Name the blood parasite species.
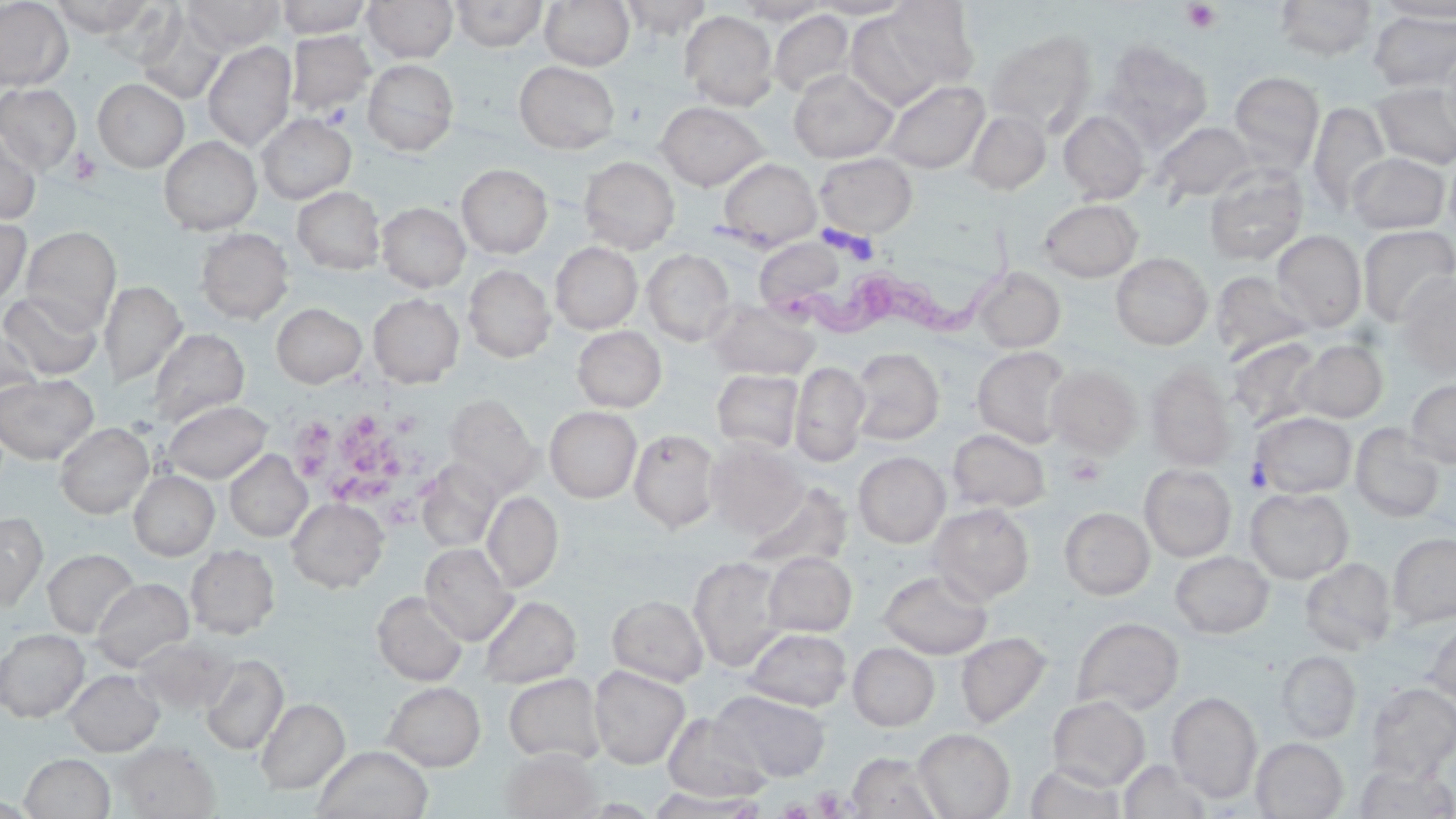

Trypanosoma brucei.

Approximate bounding boxes as (x1, y1, x2, y2) in pixels. Uninfected red blood cell locations: (0, 0, 73, 91), (50, 0, 156, 36), (183, 0, 284, 53), (274, 0, 373, 38), (363, 0, 458, 62), (451, 0, 547, 51), (540, 0, 634, 70), (619, 0, 712, 38), (808, 0, 916, 19), (881, 0, 981, 92), (1274, 0, 1377, 61), (734, 1, 831, 25), (1377, 1, 1456, 21), (844, 8, 956, 111), (768, 9, 856, 99), (1368, 9, 1456, 92), (680, 11, 778, 110), (137, 12, 227, 105), (986, 29, 1097, 136), (286, 30, 375, 116), (1102, 40, 1212, 146), (203, 41, 296, 151), (1439, 41, 1456, 145), (363, 59, 459, 155), (514, 61, 620, 153), (788, 69, 898, 163), (1229, 71, 1325, 173), (93, 79, 188, 171), (880, 79, 989, 174), (1372, 81, 1456, 169), (0, 82, 81, 172), (656, 101, 768, 190), (1308, 101, 1391, 213), (966, 109, 1051, 195), (1059, 110, 1150, 204), (257, 114, 356, 203), (1154, 121, 1256, 204), (0, 130, 41, 225), (159, 136, 261, 234), (1444, 148, 1456, 238), (1346, 152, 1451, 234), (815, 153, 917, 239), (579, 156, 679, 253), (718, 158, 821, 249), (457, 164, 553, 258), (1204, 166, 1309, 265), (293, 186, 385, 274), (1039, 199, 1142, 281), (377, 202, 470, 292), (0, 214, 31, 307), (1357, 225, 1456, 326), (21, 226, 121, 331), (196, 228, 293, 323), (1272, 230, 1367, 331), (754, 237, 849, 315), (551, 242, 642, 333), (642, 249, 735, 345), (1111, 253, 1213, 349), (463, 265, 554, 362), (972, 266, 1066, 352), (1211, 271, 1312, 360), (1395, 272, 1456, 378), (99, 280, 186, 387), (0, 291, 102, 380), (368, 293, 464, 387), (707, 300, 820, 380), (271, 302, 367, 388), (0, 325, 43, 410), (573, 326, 666, 412), (146, 328, 249, 426), (1227, 337, 1322, 429), (1293, 339, 1388, 423), (972, 346, 1072, 447), (851, 347, 944, 445), (790, 361, 869, 466), (1047, 364, 1141, 456), (1146, 364, 1235, 470), (711, 369, 804, 453), (0, 373, 98, 463), (1405, 377, 1456, 468), (445, 395, 541, 494), (163, 399, 271, 483), (545, 407, 641, 502), (1252, 411, 1356, 497), (55, 422, 153, 518), (1350, 424, 1446, 523), (947, 428, 1051, 513), (629, 429, 720, 532), (705, 439, 806, 537), (225, 451, 311, 541), (853, 451, 950, 547), (416, 460, 502, 554), (1139, 464, 1237, 561), (129, 470, 218, 560), (741, 481, 854, 574), (1245, 488, 1353, 583), (482, 491, 563, 592), (286, 497, 388, 591), (929, 503, 1034, 604), (1059, 507, 1155, 599), (0, 512, 46, 611), (1388, 532, 1456, 628), (420, 542, 516, 645), (186, 545, 280, 638), (44, 548, 138, 637), (1169, 550, 1274, 637), (764, 552, 856, 637), (689, 556, 787, 670), (1300, 557, 1396, 654), (878, 569, 993, 658), (91, 578, 193, 669), (372, 591, 468, 685), (608, 595, 708, 685), (479, 596, 581, 687), (1073, 617, 1184, 714), (1424, 620, 1456, 706), (744, 628, 851, 711), (0, 629, 89, 721), (956, 632, 1052, 729), (134, 636, 236, 715), (848, 642, 940, 730), (1276, 650, 1361, 742), (200, 654, 289, 755), (589, 665, 690, 769), (65, 670, 163, 756), (504, 673, 605, 764), (383, 682, 485, 770), (1365, 682, 1456, 779), (714, 690, 831, 782), (1167, 691, 1261, 802), (1047, 695, 1150, 790), (255, 698, 349, 793), (662, 712, 772, 802), (914, 729, 1015, 818), (1251, 737, 1348, 818), (115, 741, 219, 818), (312, 745, 433, 819), (501, 748, 601, 819), (847, 751, 943, 819), (20, 753, 115, 818), (1118, 760, 1216, 818), (1353, 762, 1456, 818), (1024, 763, 1126, 819), (647, 788, 769, 818). Trypanosoma brucei locations: (799, 219, 1020, 342). Platelet locations: (1182, 2, 1222, 34), (321, 103, 352, 129), (70, 148, 101, 185), (307, 410, 417, 511), (1065, 455, 1105, 488), (1244, 460, 1271, 492), (812, 786, 847, 816). Optical microscopy. One field of a larger specimen. May-Grünwald-Giemsa stain. Image is 1456×819 pixels. 1000x magnification. Thin blood film.